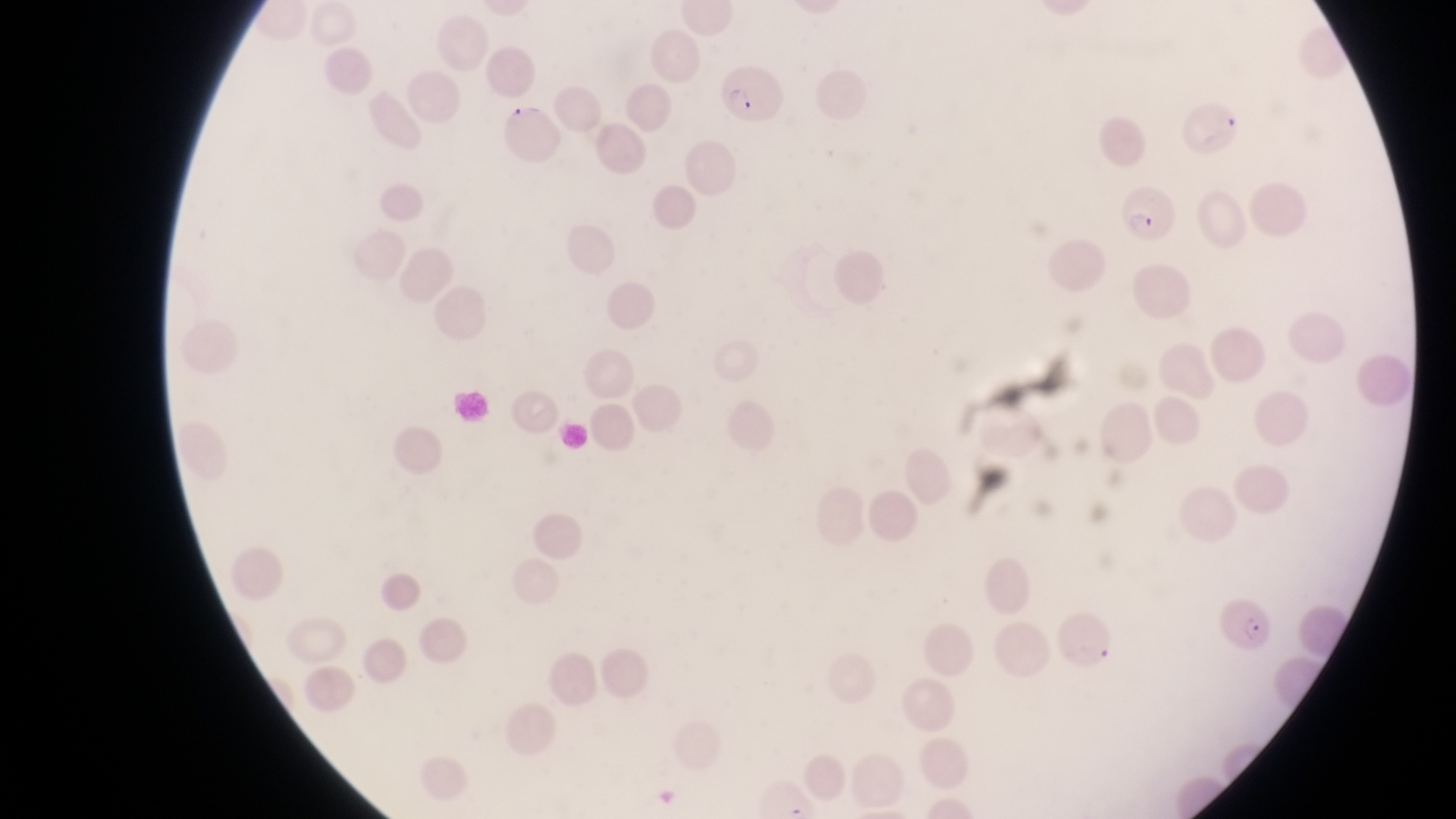
Approximate bounding boxes as (left, top, right, bottom) in pixels. Parasitised red blood cell locations: (714, 67, 781, 127), (1168, 85, 1245, 152), (497, 99, 560, 168), (1119, 184, 1179, 245), (1222, 597, 1275, 652). Leukocyte locations: (450, 384, 492, 430). Magnification of 1000x. Thin blood film. Photographed through the eyepiece of an Olympus CX-23 microscope with a smartphone camera. Image is 1456×819 pixels. Sample from Uganda. Single field of view.